Assess the morphology of the red blood cells.
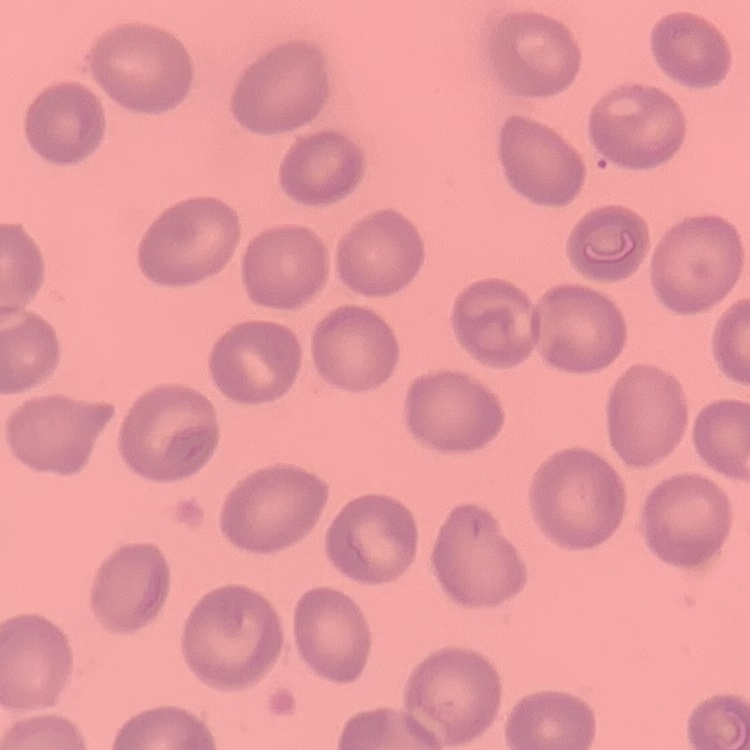

They show no rouleaux formation.

Summary:
  - Stain: Field's or Giemsa
  - Preparation: thin blood smear
  - Image type: one tile cut from a larger photomicrograph